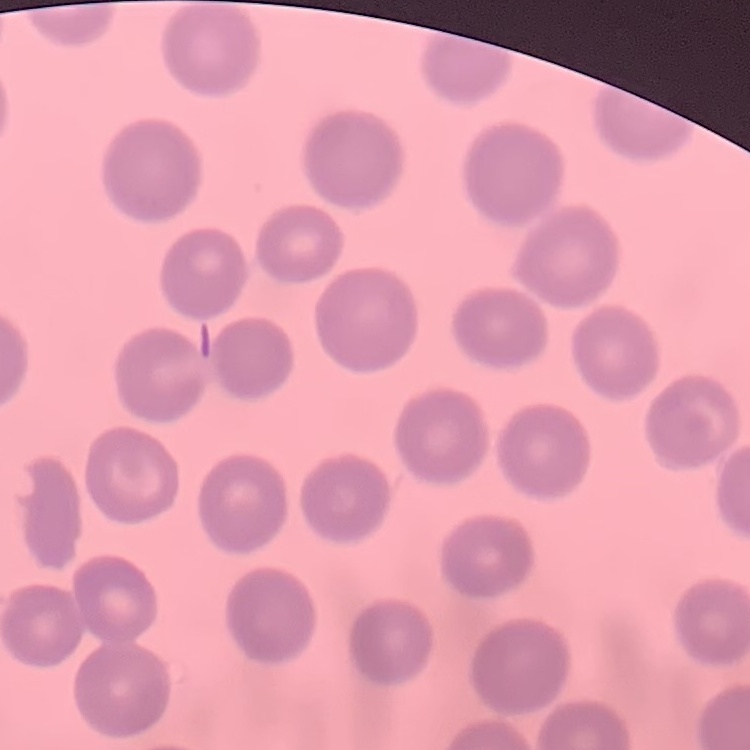

Summary:
  - Erythrocyte morphology: no rouleaux formation
  - Preparation: thin peripheral smear
  - Stain: Field's or Giemsa
  - Image type: one tile cut from a larger photomicrograph